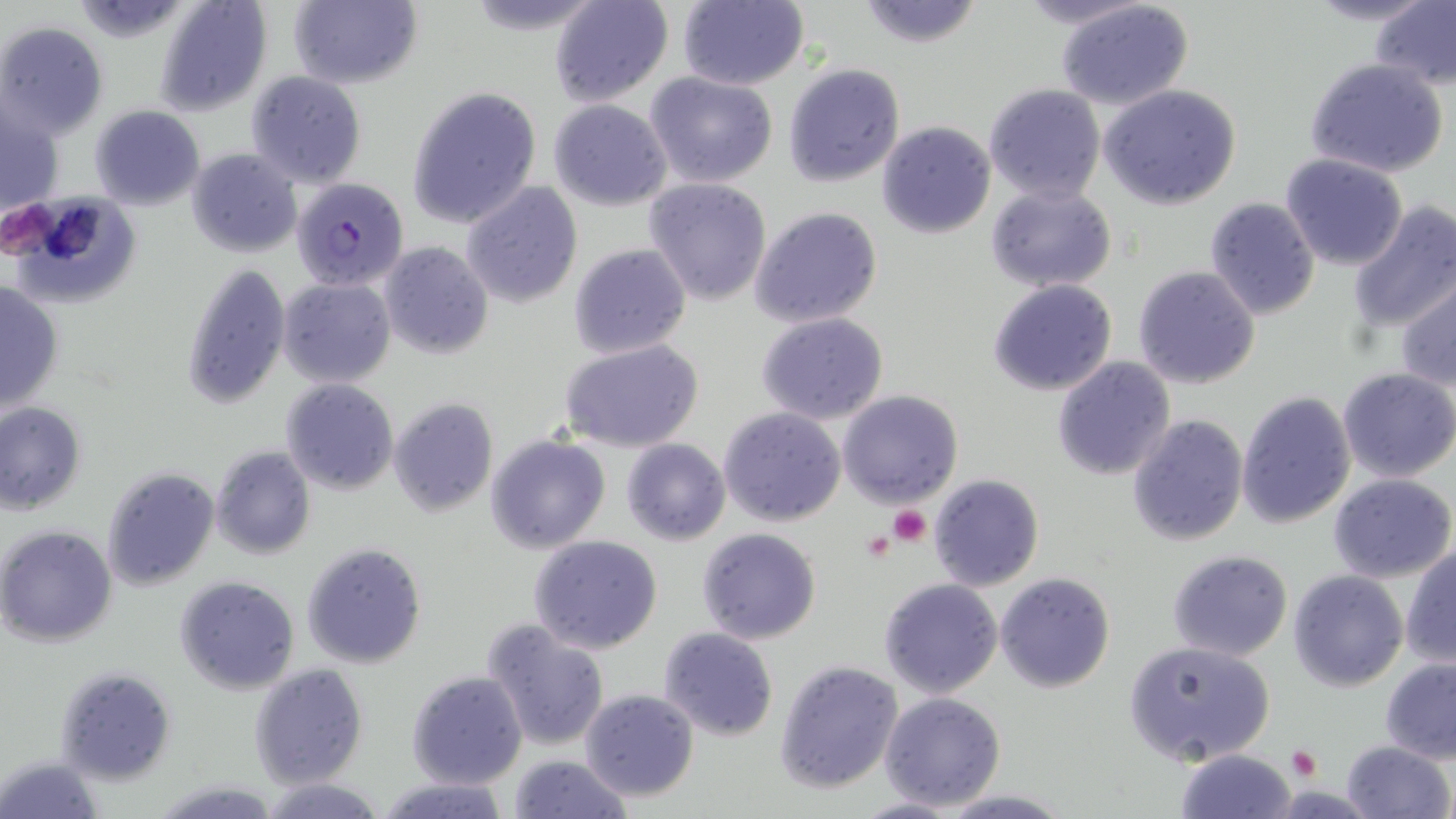 Approximate bounding boxes as (x1, y1, x2, y2) in pixels. Platelet locations: (889, 506, 931, 547), (861, 529, 894, 559), (1287, 744, 1323, 779). Plasmodium falciparum-infected red blood cell locations: (291, 177, 410, 290). Uninfected red blood cell locations: (154, 0, 273, 115), (287, 0, 423, 90), (548, 0, 674, 106), (675, 0, 811, 90), (855, 0, 987, 49), (1012, 0, 1157, 30), (1054, 0, 1197, 112), (1300, 0, 1441, 25), (1370, 0, 1456, 89), (456, 2, 609, 34), (0, 22, 107, 140), (1302, 56, 1451, 180), (783, 62, 905, 188), (246, 71, 367, 189), (646, 72, 779, 187), (1099, 83, 1242, 209), (983, 84, 1105, 204), (405, 86, 541, 229), (549, 100, 672, 210), (1, 104, 63, 220), (89, 105, 205, 210), (876, 121, 995, 238), (186, 149, 301, 257), (1280, 154, 1407, 270), (644, 177, 773, 305), (459, 182, 583, 306), (985, 183, 1118, 294), (2, 192, 142, 307), (1203, 197, 1321, 319), (1345, 201, 1456, 333), (750, 206, 883, 327), (379, 240, 497, 359), (568, 243, 692, 359), (182, 262, 291, 409), (1133, 264, 1260, 390), (1395, 273, 1456, 391), (278, 277, 397, 387), (988, 279, 1117, 396), (1, 281, 65, 413), (756, 312, 889, 425), (561, 341, 703, 453), (1051, 356, 1177, 481), (1336, 367, 1456, 481), (281, 378, 399, 494), (838, 390, 963, 509), (1235, 391, 1357, 529), (388, 397, 499, 516), (0, 401, 87, 515), (718, 407, 846, 527), (1126, 414, 1250, 546), (485, 434, 612, 555), (622, 438, 731, 546), (209, 446, 316, 561), (101, 466, 219, 591), (1328, 472, 1455, 583), (929, 473, 1044, 592), (0, 526, 119, 646), (696, 527, 822, 644), (530, 535, 662, 655), (301, 542, 427, 668), (1401, 544, 1455, 668), (1167, 549, 1293, 661), (1288, 569, 1407, 690), (995, 571, 1116, 694), (175, 575, 301, 696), (879, 577, 1002, 697), (481, 620, 610, 751), (659, 627, 779, 743), (1123, 640, 1277, 768), (1380, 657, 1456, 762), (774, 658, 903, 795), (249, 663, 370, 788), (55, 664, 177, 785), (406, 670, 527, 789), (580, 688, 701, 802), (878, 691, 1006, 811), (1340, 740, 1453, 819), (1174, 749, 1297, 819), (508, 754, 633, 818), (0, 755, 104, 819), (375, 775, 515, 819), (259, 776, 387, 818), (149, 777, 281, 818), (935, 790, 1075, 818), (849, 797, 962, 818). Slide-level diagnosis: Plasmodium falciparum. Image is 1456×819 pixels. Thin blood film. May-Grünwald-Giemsa stain. Light microscopy. 1000x magnification. Single field of view.